Locate every malaria parasite.
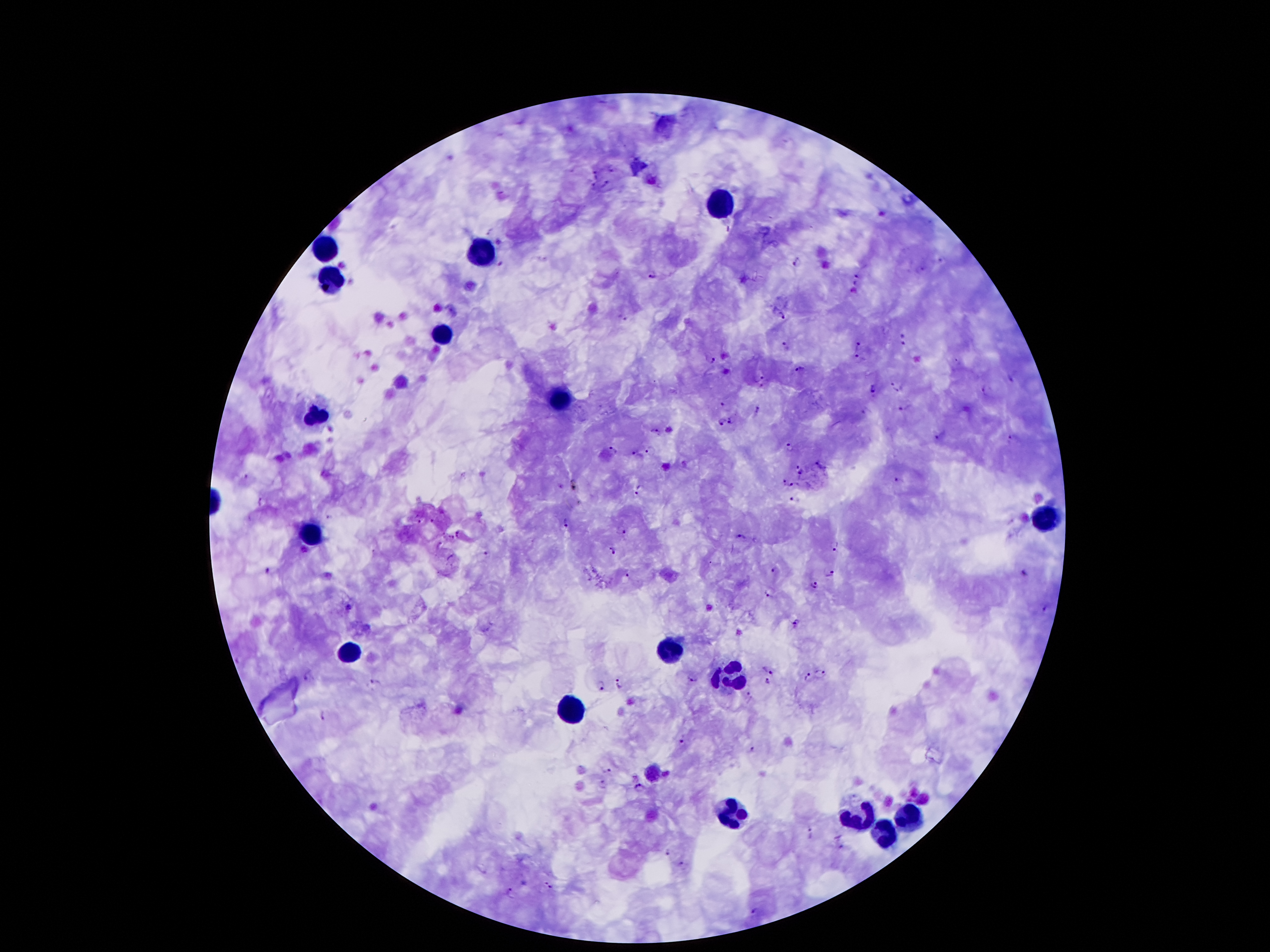
Approximate centers as {x, y} in pixels.
Malaria parasites: {612, 166}, {596, 173}, {605, 183}, {593, 186}, {490, 231}, {941, 260}, {797, 261}, {502, 263}, {921, 269}, {652, 272}, {857, 275}, {856, 282}, {854, 291}, {621, 315}, {781, 317}, {902, 333}, {902, 343}, {784, 345}, {857, 346}, {860, 358}, {710, 359}, {800, 370}, {1013, 378}, {760, 379}, {894, 386}, {873, 390}, {985, 392}, {722, 403}, {905, 406}, {758, 409}, {865, 411}, {732, 419}, {721, 422}, {655, 430}, {939, 438}, {1010, 441}, {790, 445}, {613, 450}, {651, 450}, {637, 455}, {819, 464}, {796, 466}, {800, 470}, {244, 476}, {783, 480}, {897, 480}, {576, 485}, {796, 486}, {639, 489}, {793, 496}, {262, 499}, {418, 518}, {430, 519}, {567, 522}, {622, 529}, {739, 537}, {439, 544}, {835, 545}, {488, 551}, {611, 551}, {264, 569}, {774, 570}, {626, 573}, {1024, 573}, {830, 574}, {815, 585}, {768, 591}, {347, 606}, {1045, 608}, {798, 623}, {366, 628}, {767, 669}, {309, 674}, {824, 674}, {807, 677}, {694, 679}, {374, 681}, {767, 681}, {619, 683}, {600, 686}, {749, 695}, {323, 714}, {683, 741}, {753, 748}, {605, 770}, {667, 772}, {603, 784}, {641, 789}, {811, 832}, {842, 848}, {667, 852}, {681, 863}, {549, 885}, {509, 891}, {757, 908}.

Leukocyte locations: {723, 199}, {323, 248}, {482, 252}, {332, 279}, {438, 336}, {562, 402}, {318, 416}, {1048, 517}, {307, 535}, {349, 648}, {668, 650}, {728, 674}, {573, 703}, {655, 769}, {911, 809}, {734, 811}, {860, 818}, {887, 836}. 100x magnification. Giemsa stain. Patient malaria status: positive for Plasmodium falciparum. Smartphone photograph taken through the microscope eyepiece. Thick blood film. Image is 1270×952 pixels. One field from this slide.